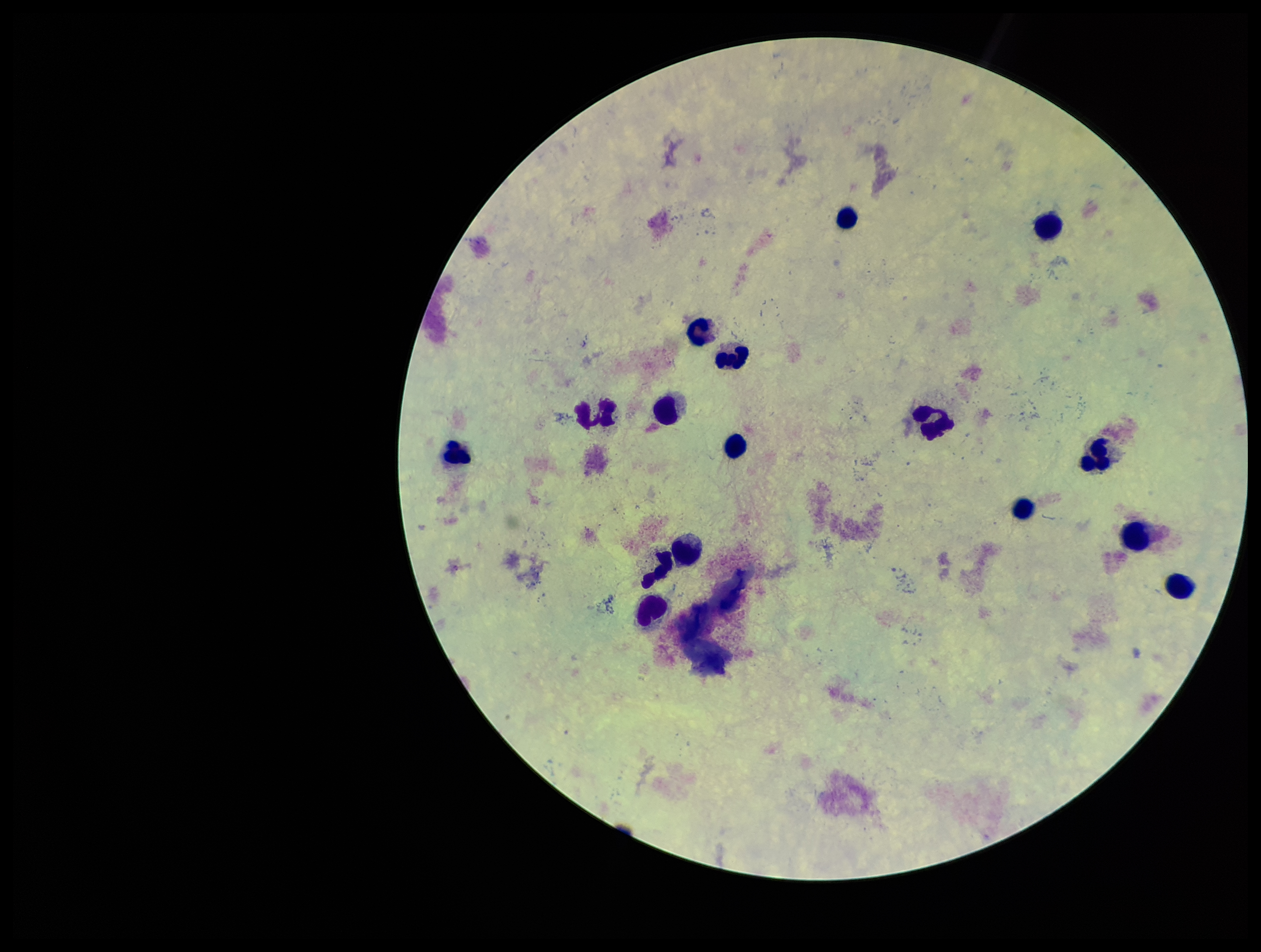
Leukocyte count: 16. Single field of view. Patient malaria status: negative. Plasmodium parasites: none detected. Parasite count: 0. Image is 1261×952 pixels. Smartphone photograph taken through the eyepiece of a microscope. Giemsa stain. Preparation: thick smear.